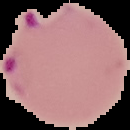

Summary:
  - Image size: 130×130 pixels
  - Preparation: thin blood smear
  - Image type: cell region segmented out of the field of view; surrounding area masked to black
  - Malaria status: parasitized